Give the preparation type.
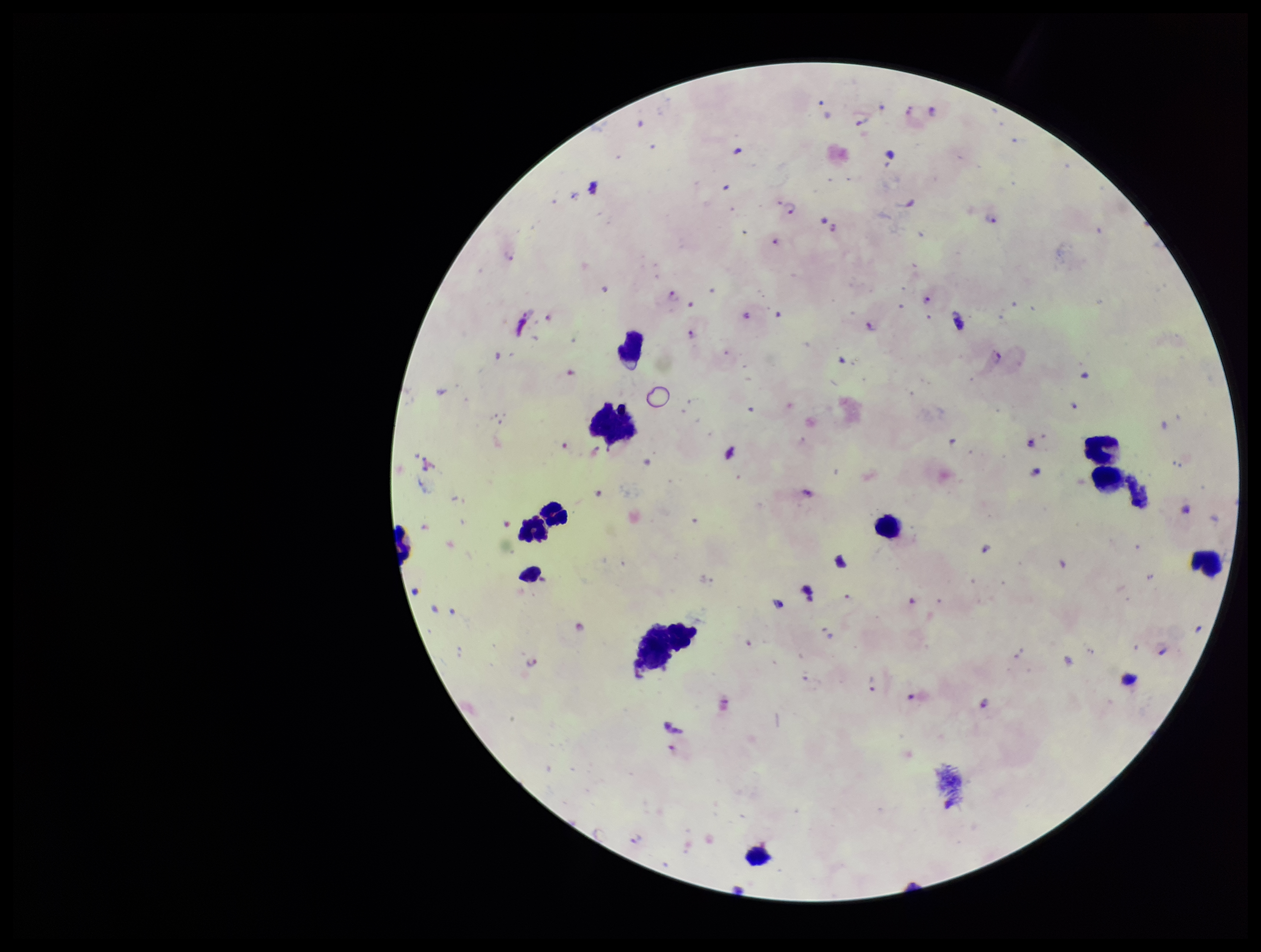

A thick smear.

Patient malaria status: positive. Leukocyte count: 10. Image is 1261×952 pixels. Species reported for this patient: Plasmodium falciparum. Parasite count: 12. One field from this slide. Plasmodium parasites: seen. Photographed through the microscope eyepiece with a smartphone camera. Stained with Giemsa.